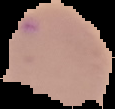

image type = cell region segmented out of the field of view; surrounding area masked to black
image size = 115×109 pixels
result = no malaria parasites detected
preparation = thin blood film